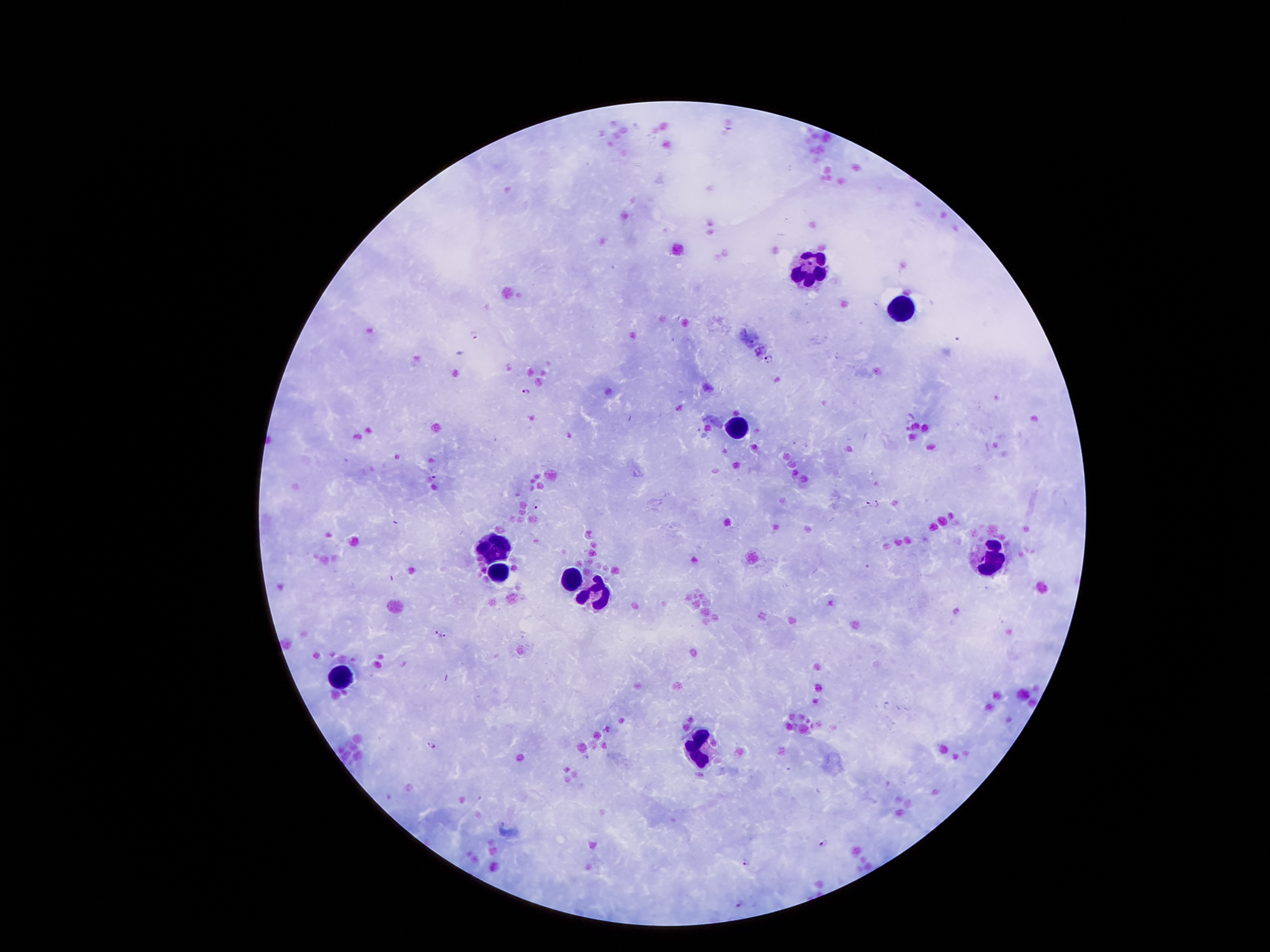

Image is 1270×952 pixels. One field from this slide. Giemsa stain. 100x magnification. Thick blood film. Photographed through the microscope eyepiece with a smartphone camera. Patient malaria status: positive for Plasmodium falciparum.